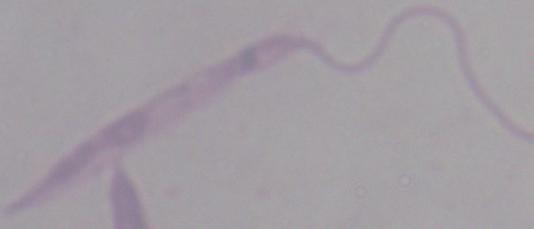
Summary:
  - Modality: micrograph
  - Magnification: 1000x
  - Identification: Leishmania